Report the malaria status of this cell.
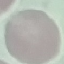
Uninfected.

{
  "preparation": "thin blood smear",
  "image_type": "cell patch, automatically extracted from a larger field of view and resized to 64 × 64 pixels",
  "stain": "Giemsa",
  "capture": "smartphone through the microscope eyepiece"
}